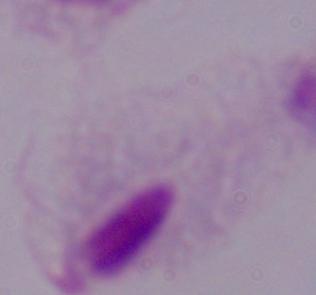
Summary:
  - Modality: photomicrograph
  - Magnification: 1000x
  - Identification: trichomonad